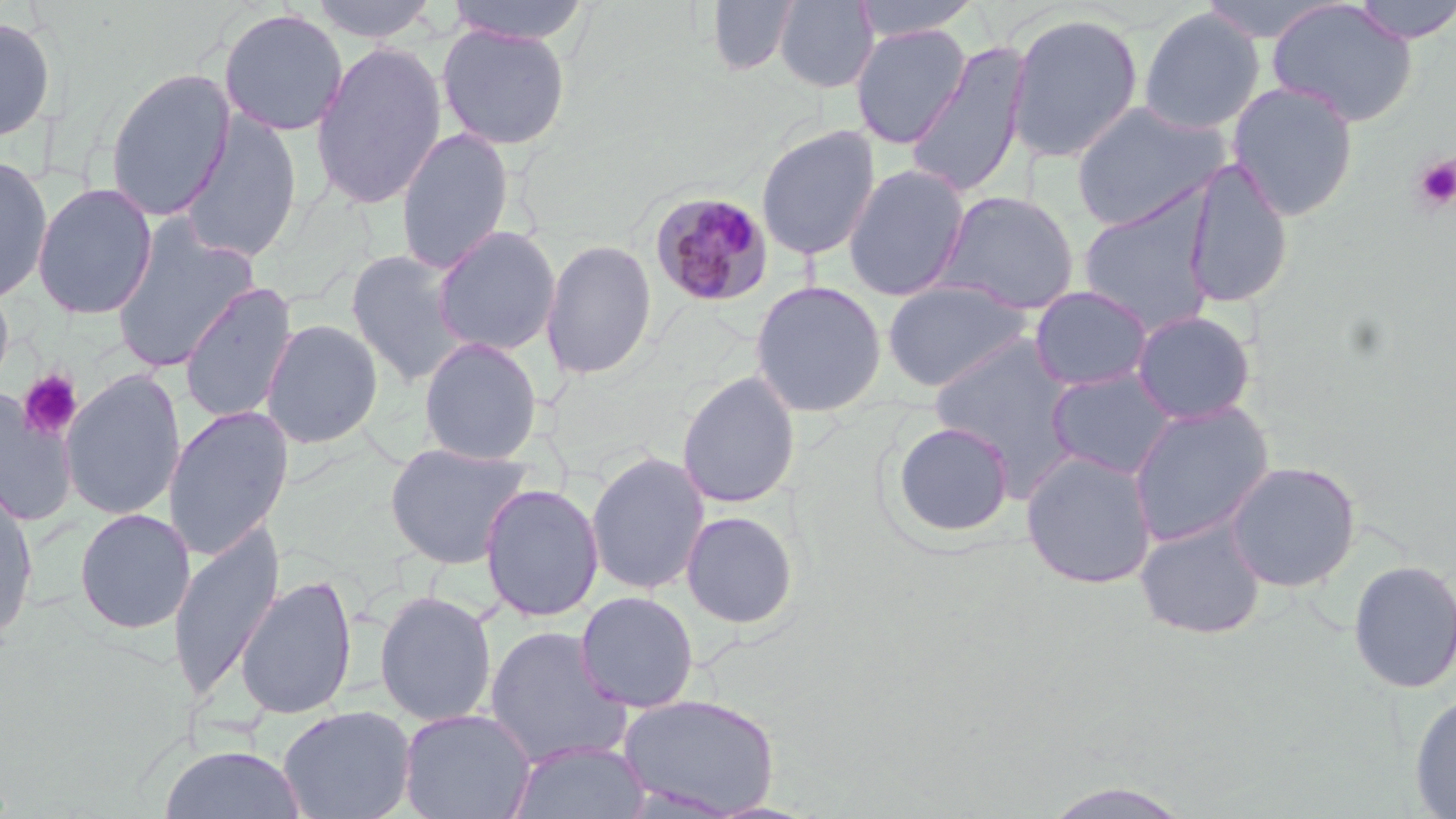
Summary:
  - Coordinate format: approximate bounding boxes as (x1, y1, x2, y2) in pixels
  - Uninfected red blood cell locations: (310, 0, 438, 43), (445, 0, 593, 45), (705, 0, 800, 76), (774, 0, 879, 92), (851, 0, 983, 40), (1197, 0, 1345, 43), (1347, 0, 1456, 44), (1266, 1, 1418, 128), (218, 8, 348, 137), (1138, 8, 1264, 135), (1007, 12, 1144, 162), (0, 17, 57, 142), (849, 23, 972, 149), (436, 24, 571, 150), (310, 41, 448, 210), (905, 41, 1032, 199), (104, 67, 236, 221), (1226, 81, 1360, 220), (1070, 100, 1232, 231), (177, 109, 304, 265), (756, 124, 881, 262), (396, 126, 514, 274), (0, 154, 53, 304), (1182, 158, 1294, 310), (843, 163, 970, 302), (32, 183, 157, 320), (933, 190, 1081, 315), (1077, 192, 1218, 335), (110, 220, 259, 374), (432, 226, 561, 356), (541, 239, 657, 380), (344, 249, 470, 387), (882, 278, 1035, 391), (749, 280, 887, 417), (179, 281, 299, 424), (1029, 285, 1153, 392), (1132, 309, 1257, 425), (260, 318, 383, 449), (928, 334, 1077, 471), (418, 336, 543, 465), (1045, 367, 1179, 480), (60, 368, 186, 521), (677, 371, 801, 509), (0, 388, 77, 527), (1127, 401, 1274, 548), (163, 406, 294, 561), (891, 422, 1015, 539), (384, 441, 533, 570), (1020, 450, 1158, 589), (586, 451, 709, 595), (1224, 460, 1361, 592), (480, 483, 603, 622), (0, 484, 39, 644), (74, 508, 195, 635), (681, 509, 799, 629), (1134, 518, 1267, 639), (168, 522, 285, 702), (1347, 558, 1456, 695), (235, 574, 358, 719), (374, 590, 497, 726), (574, 591, 700, 712), (484, 625, 632, 767), (1408, 689, 1456, 818), (618, 692, 780, 816), (277, 704, 417, 819), (398, 708, 536, 819), (508, 739, 651, 819), (158, 744, 306, 819)
  - Platelet locations: (1412, 154, 1456, 212), (18, 369, 83, 441)
  - Plasmodium malariae-infected red blood cell locations: (649, 190, 774, 308)
  - Slide-level diagnosis: Plasmodium malariae
  - Modality: light microscopy
  - Stain: May-Grünwald-Giemsa
  - Image size: 1456×819 pixels
  - Field of view: one of a larger specimen
  - Magnification: 1000x
  - Preparation: thin blood smear